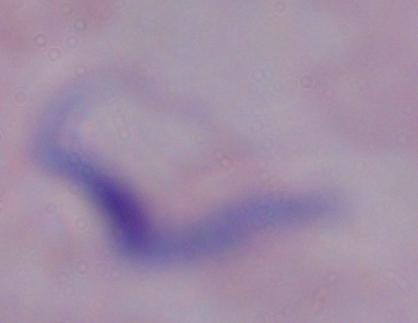

A trypanosome is shown. Micrograph. Captured at 1000x magnification.